Give the position of every malaria parasite.
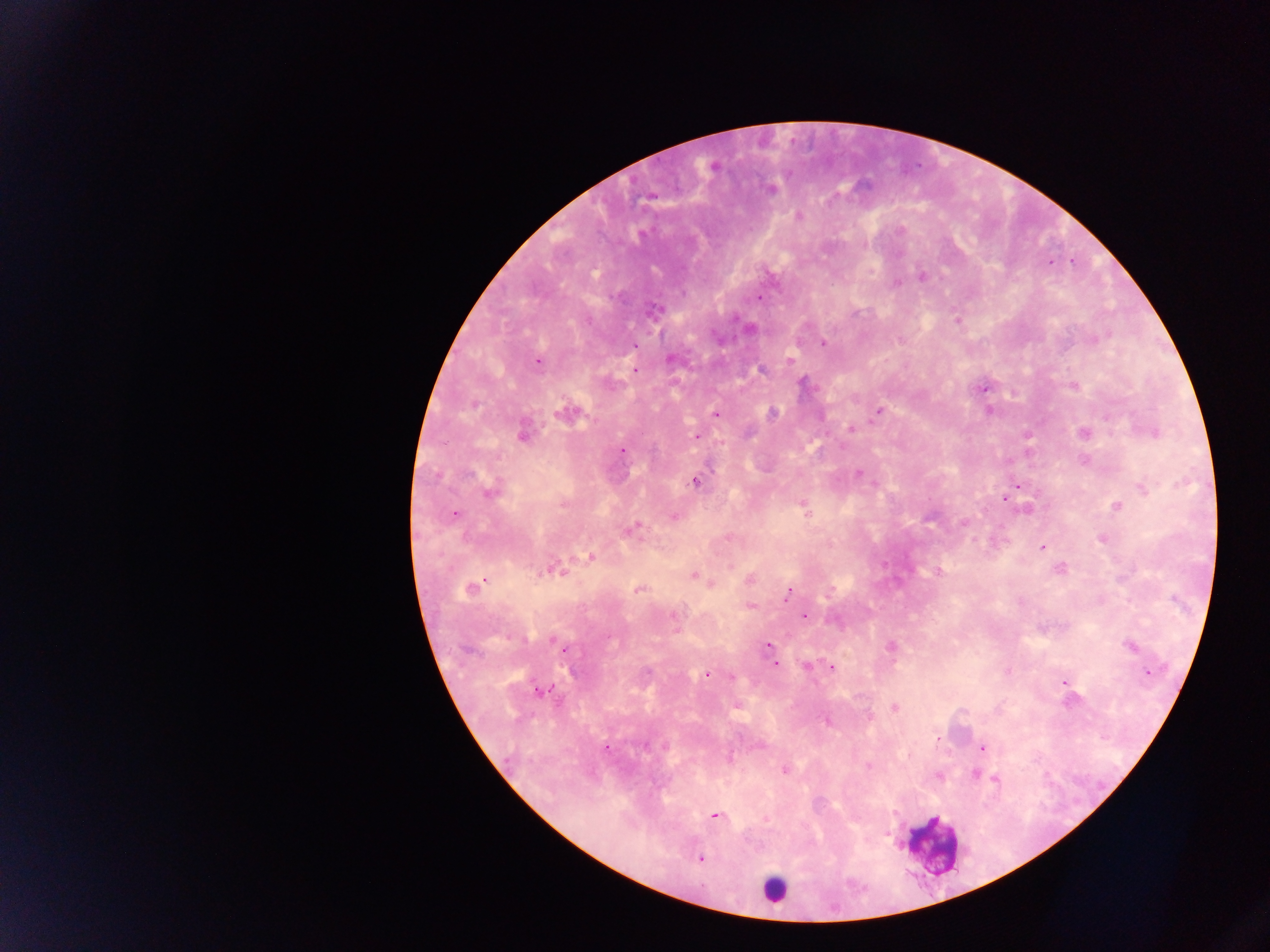
Approximate centers as x y in pixels.
Malaria parasites: 713 165; 770 189; 797 216; 1071 262; 921 276; 895 282; 758 297; 652 310; 957 320; 749 328; 823 344; 671 358; 791 360; 536 361; 634 370; 761 370; 803 384; 1074 386; 983 388; 988 409; 877 411; 567 412; 773 413; 715 414; 851 429; 1153 431; 522 433; 1083 433; 1026 435; 697 437; 621 450; 1083 460; 859 473; 695 481; 874 485; 1017 485; 1142 489; 489 492; 1005 496; 802 505; 1117 505; 454 513; 673 517; 963 523; 631 528; 1102 539; 1043 547; 589 556; 1061 568; 552 569; 938 571; 694 575; 750 580; 710 582; 471 588; 638 589; 789 593; 750 606; 803 615; 559 643; 767 645; 1130 645; 890 646; 562 648; 770 648; 774 663; 807 665; 826 666; 831 668; 1008 670; 1147 672; 706 674; 731 676; 1064 681; 1066 688; 538 690; 894 708; 826 720; 982 748; 605 749; 868 765; 783 770; 974 773; 938 775; 996 780; 715 815; 766 819; 701 859.

Summary:
  - Leukocyte locations: 932 846; 774 888
  - Country: Ghana
  - Capture: mobile-phone photograph through a microscope
  - Preparation: thick blood smear
  - Image size: 1270×952 pixels
  - Field of view: single